Evaluate for Plasmodium parasites.
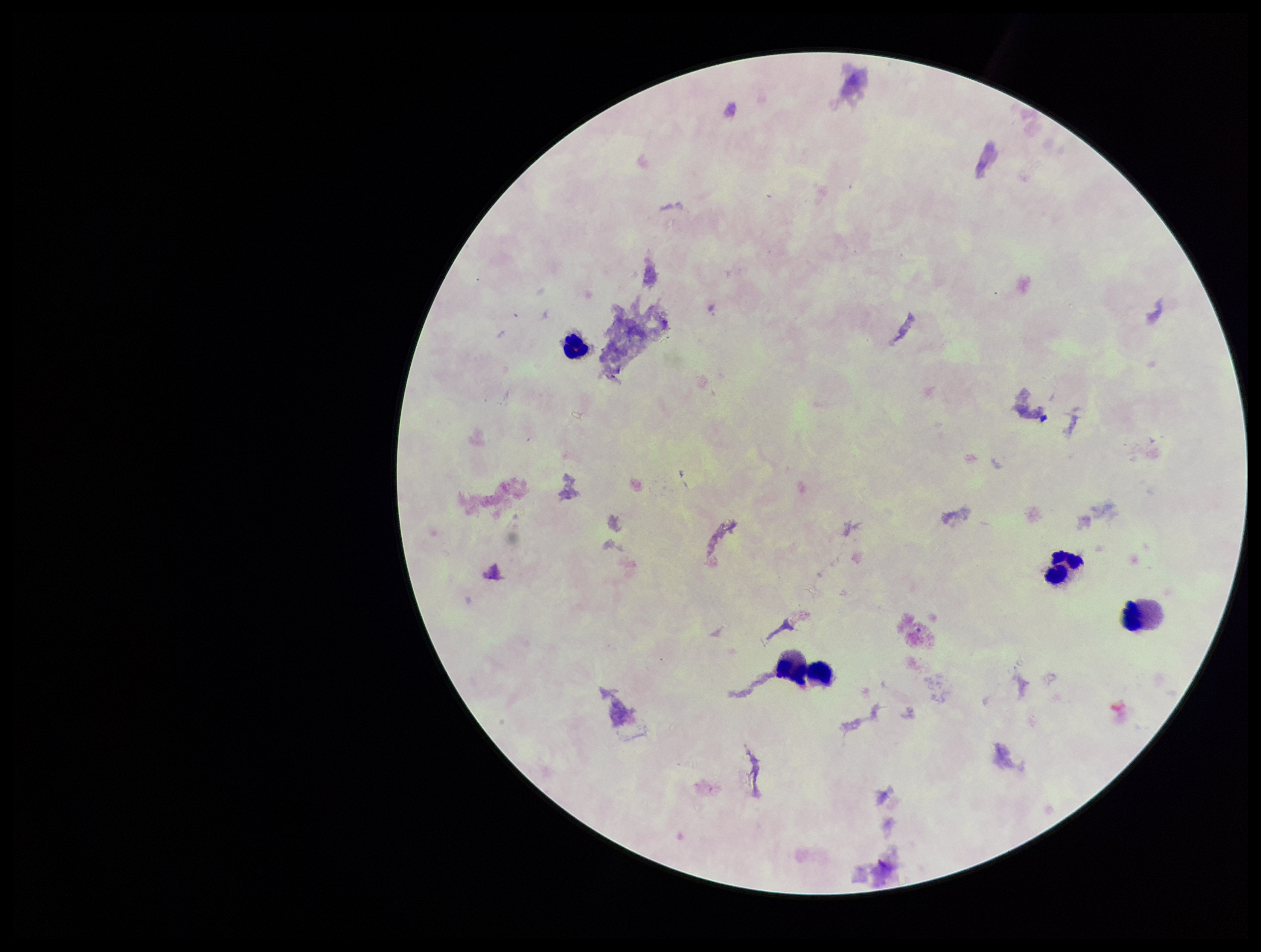
None detected.

patient malaria status = negative
parasite count = 0
capture = smartphone photograph through the microscope eyepiece
image size = 1261×952 pixels
preparation = thick
leukocyte count = 4
stain = Giemsa
field of view = one from this slide